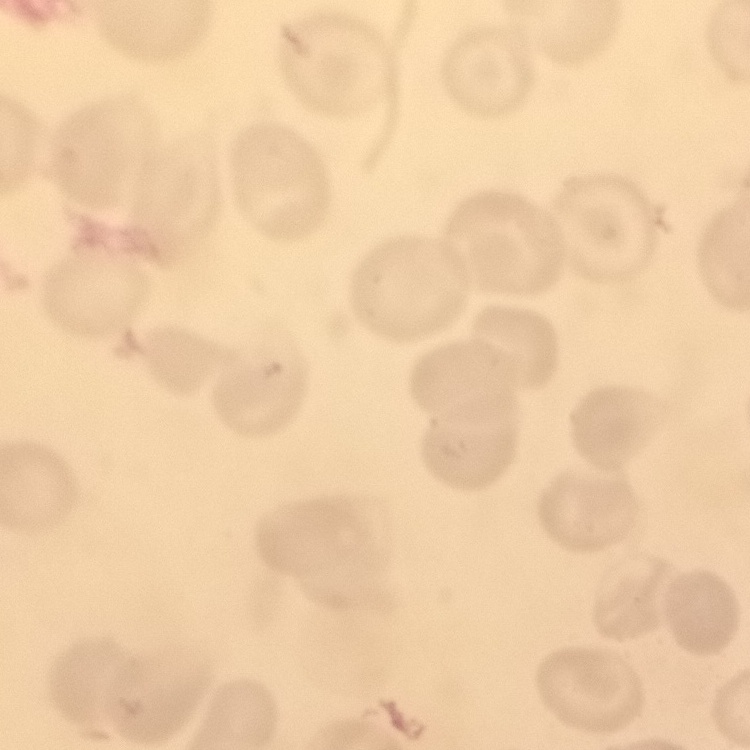

Summary:
  - Erythrocyte morphology: no rouleaux formation
  - Stain: Field's or Giemsa
  - Preparation: thin blood film
  - Image type: square crop of a larger photomicrograph